Assess the morphology of the erythrocytes.
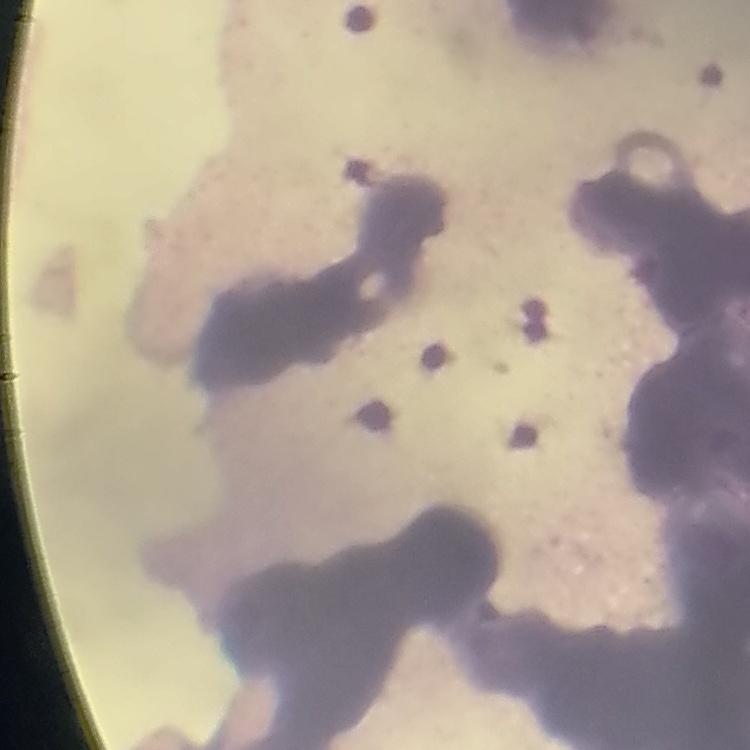
They show rouleaux formation.

Thin peripheral smear. Field's or Giemsa stain. One tile cut from a larger photomicrograph.